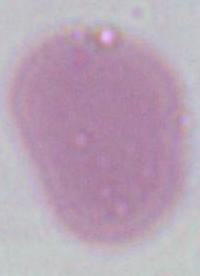

{
  "identification": "red blood cell",
  "modality": "photomicrograph",
  "magnification": "1000x"
}